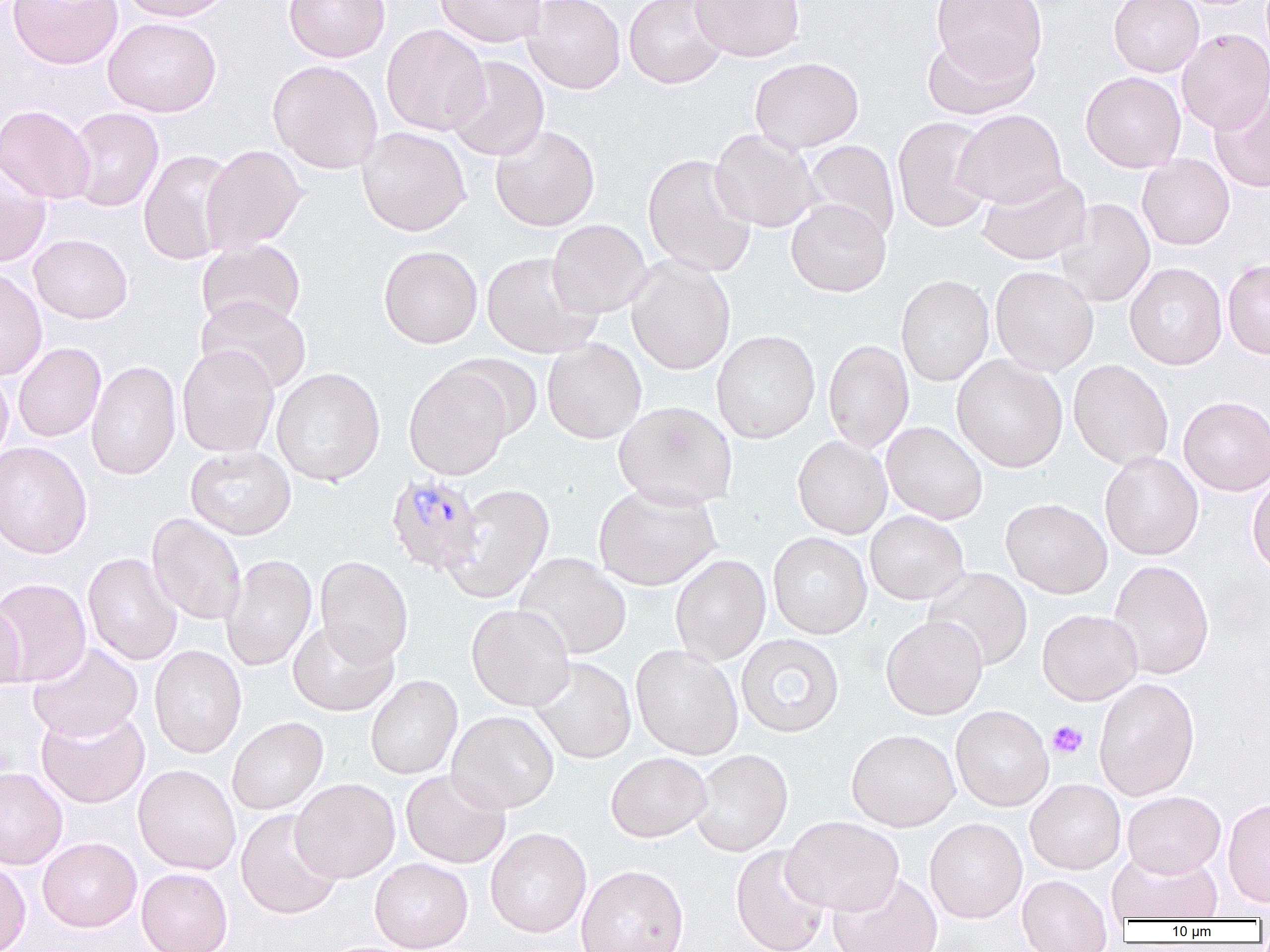

slide-level diagnosis = Plasmodium malariae
modality = light microscopy
magnification = 1000x
field of view = single
uninfected red blood cell locations = approximate bounding boxes as (x1,y1)-(x2,y2) corner pairs in pixels: (7,0)-(123,69), (116,0)-(235,22), (283,0)-(390,62), (434,0)-(547,48), (523,0)-(625,94), (690,0)-(805,62), (930,0)-(1047,83), (1108,0)-(1204,77), (624,1)-(728,89), (102,16)-(221,117), (382,24)-(490,136), (1176,29)-(1270,133), (921,33)-(1038,120), (445,55)-(549,161), (750,57)-(864,153), (267,60)-(384,173), (1081,71)-(1186,172), (1209,92)-(1270,194), (0,104)-(96,204), (66,107)-(164,212), (954,109)-(1068,208), (892,116)-(995,233), (490,124)-(600,232), (357,126)-(470,236), (710,129)-(822,233), (803,140)-(900,243), (201,145)-(307,254), (138,150)-(237,265), (643,154)-(757,277), (1137,154)-(1235,250), (0,165)-(51,268), (977,171)-(1092,265), (786,199)-(891,297), (1055,199)-(1155,307), (547,219)-(652,318), (29,234)-(133,324), (196,238)-(306,331), (378,245)-(483,349), (481,251)-(601,358), (626,256)-(736,375), (1223,259)-(1270,360), (1125,262)-(1227,369), (990,265)-(1098,375), (0,267)-(47,382), (896,274)-(994,387), (196,295)-(311,394), (711,330)-(820,444), (542,338)-(646,444), (823,339)-(914,453), (13,342)-(106,442), (177,345)-(279,457), (442,354)-(544,441), (952,355)-(1068,473), (1068,359)-(1173,470), (86,360)-(181,480), (404,364)-(513,481), (0,367)-(13,465), (272,368)-(385,486), (1178,396)-(1270,495), (613,401)-(738,509), (881,422)-(988,524), (792,435)-(892,539), (0,441)-(92,559), (186,445)-(296,540), (1100,451)-(1204,560), (1246,473)-(1270,578), (445,483)-(554,603), (593,483)-(721,591), (1001,498)-(1112,599), (865,511)-(969,605), (148,513)-(246,625), (768,532)-(872,639), (83,552)-(182,666), (514,552)-(631,660), (222,554)-(317,671), (670,554)-(771,665), (315,556)-(413,667), (1108,559)-(1215,680), (923,567)-(1032,671), (0,578)-(91,686), (0,599)-(25,691), (466,603)-(575,711), (1037,609)-(1142,705), (881,615)-(988,719), (287,620)-(398,716), (735,633)-(845,738), (28,643)-(143,741), (149,645)-(246,758), (631,645)-(743,760), (529,656)-(637,764), (365,675)-(462,780), (1093,677)-(1200,801), (950,705)-(1054,812), (36,707)-(149,808), (447,710)-(559,813), (227,716)-(328,814), (846,729)-(960,831), (690,749)-(793,857), (605,752)-(711,842), (133,764)-(241,875), (0,767)-(67,870), (401,770)-(510,868), (291,778)-(400,882), (1025,778)-(1126,874), (1122,791)-(1225,878), (1223,797)-(1270,909), (236,809)-(344,919), (781,816)-(904,916), (924,817)-(1027,923), (485,827)-(591,938), (37,837)-(142,932), (730,844)-(831,952), (1107,849)-(1223,923), (370,857)-(473,952), (0,859)-(31,952), (576,865)-(689,952), (136,867)-(233,952), (828,873)-(943,952), (1017,874)-(1113,951)
image size = 1270×952 pixels
preparation = thin blood smear
platelet locations = approximate bounding boxes as (x1,y1)-(x2,y2) corner pairs in pixels: (1047,720)-(1087,758)
Plasmodium malariae-infected red blood cell locations = approximate bounding boxes as (x1,y1)-(x2,y2) corner pairs in pixels: (389,476)-(487,580)